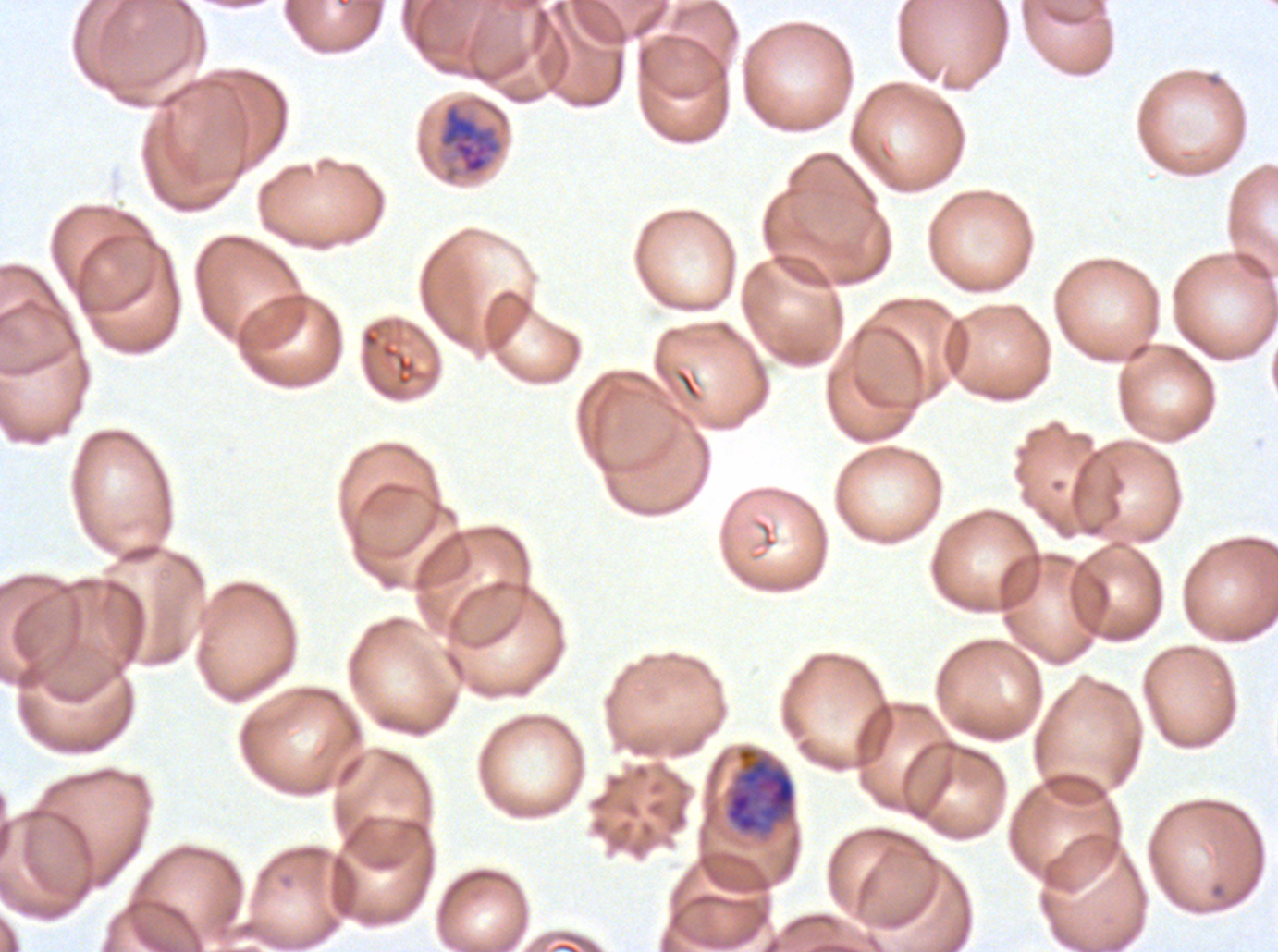 Approximate bounding boxes as (x1, y1, x2, y2) in pixels. Early schizont locations: (724, 746, 796, 836). Mid trophozoite locations: (436, 100, 505, 182). Giemsa stain. P. falciparum cultured ex vivo for 24 to 48 hours, from a patient in The Gambia. Thin blood smear. Life-cycle stages observed: mid trophozoite, early schizont. One sub-image of a larger composite. Image is 1278×952 pixels.